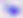

Summary:
  - Identification: Toxoplasma gondii
  - Modality: photomicrograph
  - Magnification: 400x